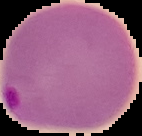
Summary:
  - Malaria status: parasitized
  - Image type: segmented cell region on a black background
  - Image size: 142×136 pixels
  - Preparation: thin blood film